Locate and identify every blood parasite.
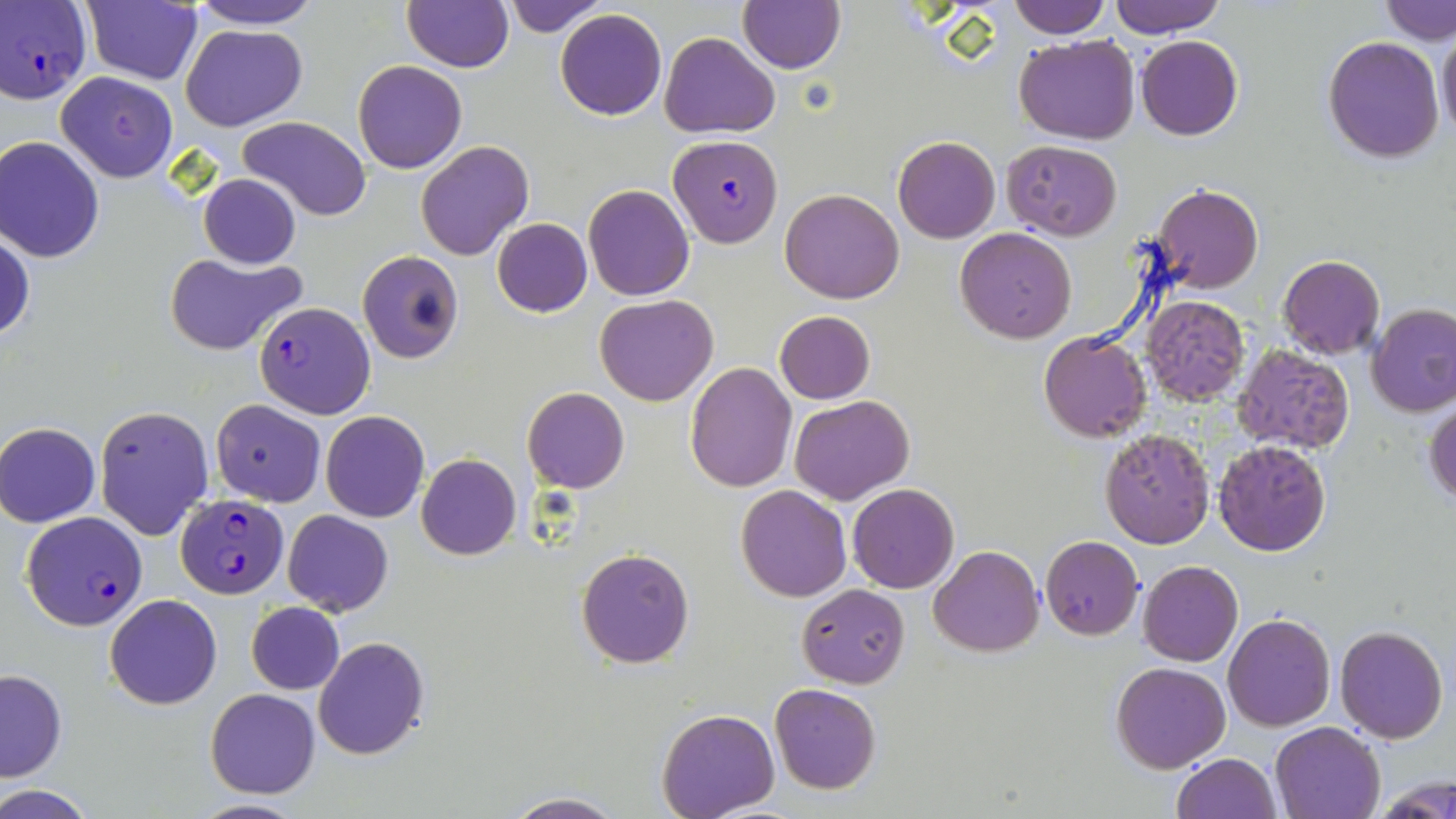

Approximate bounding boxes as named x1/y1/x2/y2 corners in pixels.
Plasmodium falciparum-infected red blood cells: (x1=0, y1=2, x2=91, y2=103), (x1=668, y1=135, x2=782, y2=248), (x1=253, y1=301, x2=376, y2=419), (x1=175, y1=493, x2=286, y2=596), (x1=19, y1=510, x2=149, y2=631).
No Plasmodium ovale, Plasmodium malariae, Plasmodium vivax, Babesia divergens, or Trypanosoma brucei observed.

Uninfected red blood cell locations: (x1=80, y1=0, x2=203, y2=86), (x1=187, y1=0, x2=324, y2=28), (x1=501, y1=0, x2=606, y2=36), (x1=1109, y1=0, x2=1228, y2=36), (x1=1379, y1=0, x2=1455, y2=47), (x1=401, y1=1, x2=513, y2=72), (x1=737, y1=1, x2=847, y2=74), (x1=1007, y1=1, x2=1110, y2=39), (x1=555, y1=8, x2=667, y2=120), (x1=181, y1=24, x2=306, y2=130), (x1=1437, y1=26, x2=1456, y2=144), (x1=661, y1=32, x2=780, y2=139), (x1=1014, y1=34, x2=1140, y2=145), (x1=1135, y1=35, x2=1243, y2=139), (x1=1323, y1=36, x2=1446, y2=164), (x1=353, y1=60, x2=467, y2=173), (x1=56, y1=71, x2=178, y2=183), (x1=237, y1=116, x2=370, y2=222), (x1=892, y1=135, x2=1001, y2=244), (x1=0, y1=137, x2=105, y2=262), (x1=416, y1=140, x2=533, y2=261), (x1=1002, y1=140, x2=1122, y2=240), (x1=199, y1=175, x2=301, y2=269), (x1=582, y1=182, x2=695, y2=301), (x1=1151, y1=182, x2=1264, y2=296), (x1=780, y1=188, x2=905, y2=304), (x1=491, y1=218, x2=592, y2=317), (x1=954, y1=228, x2=1078, y2=345), (x1=1, y1=231, x2=34, y2=345), (x1=163, y1=252, x2=306, y2=355), (x1=358, y1=252, x2=463, y2=364), (x1=1277, y1=254, x2=1385, y2=359), (x1=595, y1=294, x2=718, y2=407), (x1=1139, y1=294, x2=1250, y2=408), (x1=1366, y1=304, x2=1456, y2=417), (x1=773, y1=310, x2=875, y2=403), (x1=1038, y1=332, x2=1152, y2=441), (x1=1231, y1=344, x2=1357, y2=455), (x1=684, y1=362, x2=796, y2=491), (x1=523, y1=387, x2=629, y2=494), (x1=789, y1=394, x2=915, y2=504), (x1=1425, y1=398, x2=1456, y2=508), (x1=209, y1=399, x2=325, y2=506), (x1=95, y1=405, x2=214, y2=539), (x1=319, y1=410, x2=430, y2=522), (x1=1, y1=422, x2=100, y2=526), (x1=1100, y1=429, x2=1214, y2=548), (x1=1211, y1=438, x2=1332, y2=557), (x1=416, y1=454, x2=522, y2=560), (x1=847, y1=483, x2=960, y2=594), (x1=735, y1=484, x2=853, y2=602), (x1=281, y1=509, x2=393, y2=616), (x1=1040, y1=535, x2=1144, y2=639), (x1=929, y1=544, x2=1043, y2=657), (x1=577, y1=547, x2=694, y2=668), (x1=1138, y1=560, x2=1243, y2=667), (x1=797, y1=584, x2=909, y2=689), (x1=104, y1=594, x2=222, y2=709), (x1=246, y1=601, x2=344, y2=695), (x1=1223, y1=612, x2=1335, y2=731), (x1=1334, y1=625, x2=1448, y2=744), (x1=313, y1=637, x2=430, y2=758), (x1=1111, y1=662, x2=1230, y2=773), (x1=1, y1=668, x2=68, y2=782), (x1=770, y1=683, x2=881, y2=795), (x1=204, y1=687, x2=321, y2=799), (x1=656, y1=709, x2=780, y2=818), (x1=1269, y1=720, x2=1387, y2=818), (x1=1171, y1=752, x2=1282, y2=819), (x1=1374, y1=782, x2=1454, y2=818), (x1=0, y1=787, x2=95, y2=818), (x1=503, y1=793, x2=627, y2=819), (x1=189, y1=800, x2=308, y2=819). Slide-level diagnosis: Plasmodium falciparum. Thin blood smear. Image is 1456×819 pixels. Light microscopy. Single field of view. May-Grünwald-Giemsa-stained preparation. Captured at 1000x magnification.